Assess the background quality.
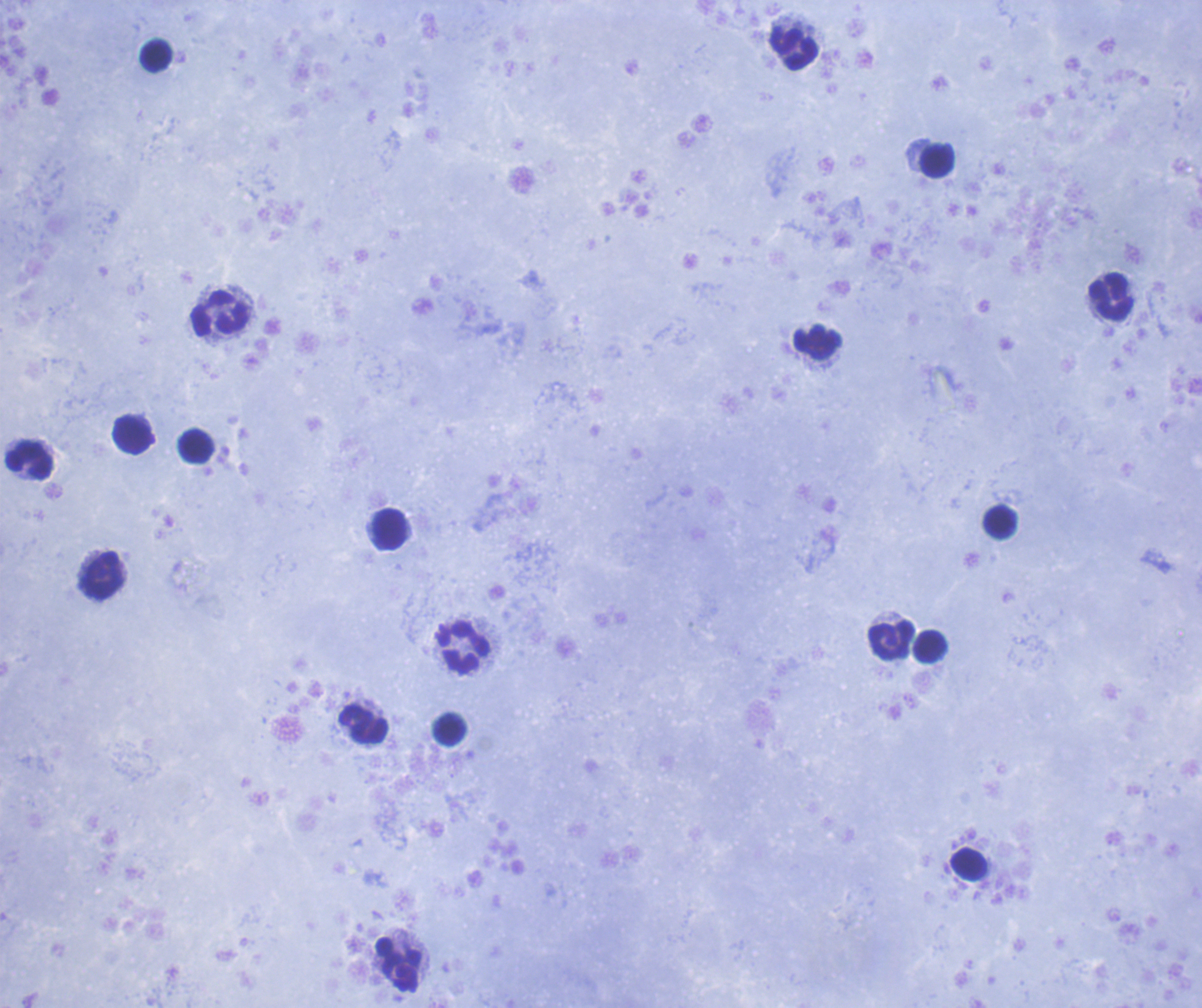

Satisfactory.

Approximate centers as (x, y) in pixels. Leukocyte locations: (794, 48), (157, 55), (937, 160), (1111, 296), (220, 313), (818, 342), (132, 434), (196, 445), (30, 460), (1000, 521), (390, 530), (102, 575), (891, 640), (931, 647), (463, 649), (363, 725), (448, 730), (969, 864). 100x magnification. Previously used in an actual diagnosis. Coloration quality: good. Result: no Plasmodium parasites detected. Image is 1202×1008 pixels. One field from this slide. Romanowsky stain. Thick blood smear.